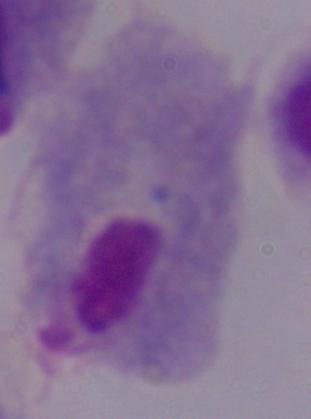
magnification = 1000x
modality = micrograph
identification = trichomonad